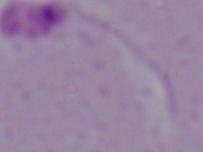
Summary:
  - Identification: Leishmania
  - Magnification: 1000x
  - Modality: micrograph